Name the cell type shown.
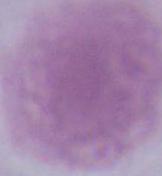
An erythrocyte.

{
  "magnification": "1000x",
  "modality": "micrograph"
}